Classify this cell by malaria status.
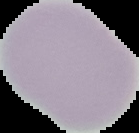

It is uninfected.

From a thin blood film. The area outside the segmented cell region is set to black. Image is 139×133 pixels.